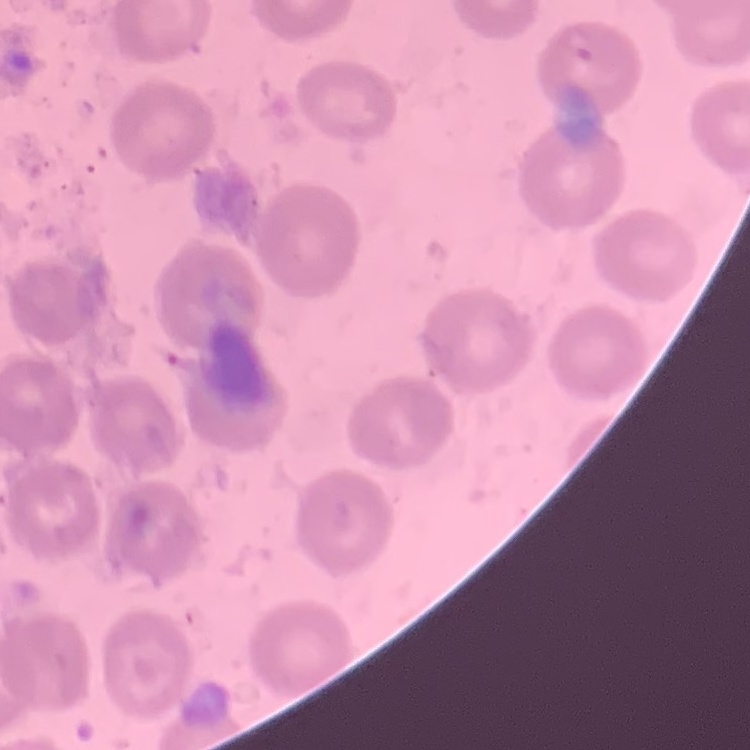 The red blood cells show no rouleaux formation. Thin blood smear. One tile cut from a larger photomicrograph. Field's or Giemsa stain.